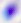
magnification: 400x
modality: micrograph
identification: Toxoplasma gondii